Name the blood parasite species.
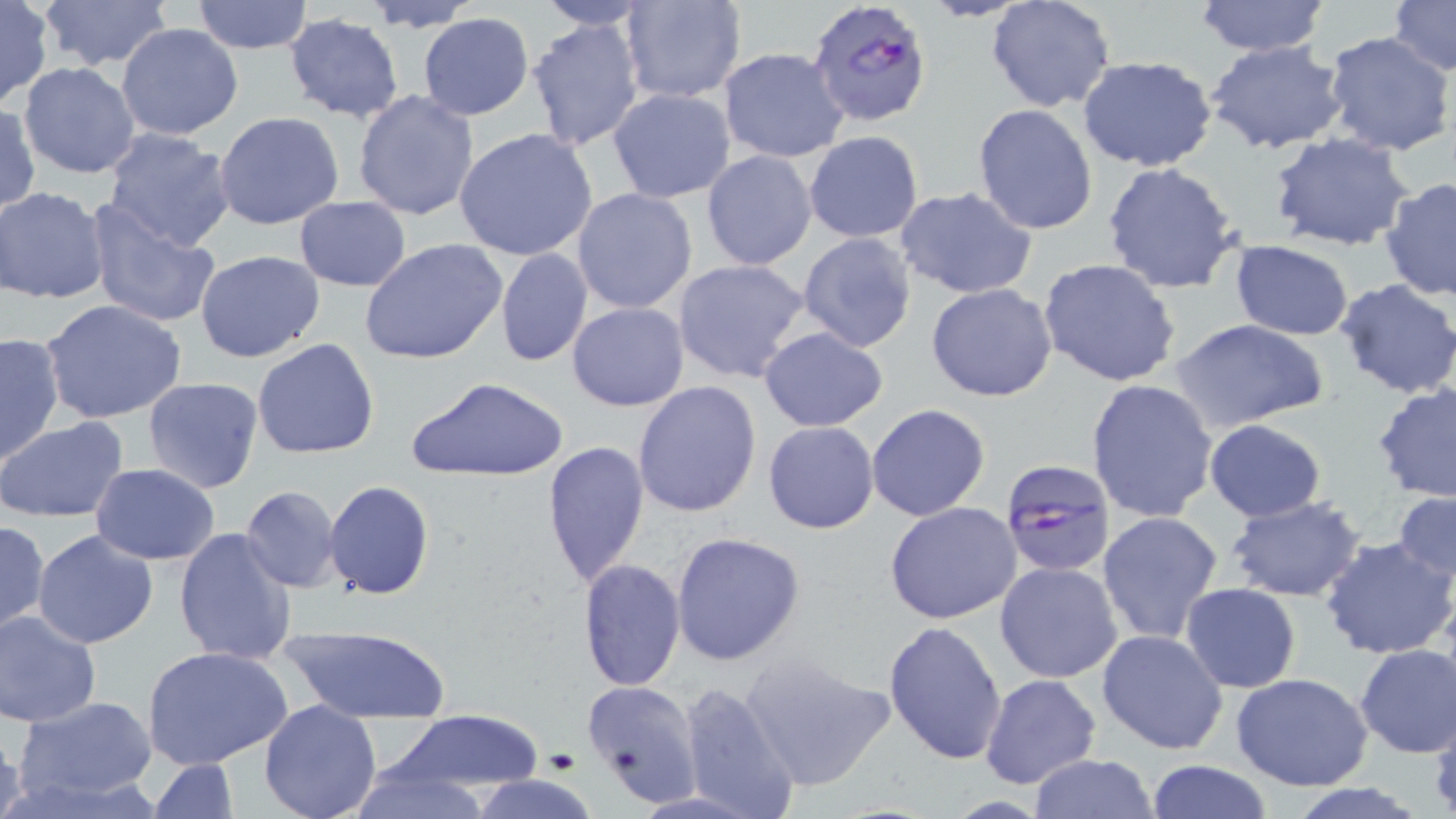

Plasmodium falciparum.

magnification = 1000x
field of view = one of a larger specimen
uninfected red blood cell locations = approximate bounding boxes as (x1,y1)-(x2,y2) corner pairs in pixels: (35,0)-(174,70), (534,0)-(655,30), (619,0)-(747,103), (985,0)-(1116,114), (1192,0)-(1331,56), (1386,0)-(1455,74), (192,1)-(312,52), (362,1)-(482,32), (0,3)-(50,106), (416,12)-(534,120), (283,15)-(406,123), (526,16)-(644,154), (117,21)-(244,142), (1323,32)-(1456,158), (1205,39)-(1348,155), (719,48)-(849,162), (1076,54)-(1219,172), (19,62)-(141,180), (607,88)-(737,204), (353,90)-(479,220), (972,103)-(1099,235), (1,105)-(40,216), (214,112)-(345,230), (454,127)-(597,262), (102,128)-(236,252), (805,131)-(923,242), (1266,131)-(1415,253), (701,150)-(818,271), (1101,161)-(1244,296), (1379,177)-(1456,301), (1,185)-(111,305), (896,185)-(1038,301), (571,187)-(698,315), (294,197)-(411,290), (84,202)-(221,328), (798,231)-(919,353), (360,237)-(507,365), (1229,240)-(1355,340), (495,249)-(593,366), (195,250)-(327,363), (672,258)-(811,384), (1037,258)-(1183,388), (1334,278)-(1456,399), (926,283)-(1058,403), (41,300)-(189,424), (567,302)-(689,411), (1170,318)-(1328,432), (758,327)-(889,432), (0,331)-(65,466), (252,338)-(380,459), (407,376)-(568,480), (142,377)-(266,495), (1086,379)-(1220,524), (632,381)-(762,520), (1370,382)-(1456,501), (867,402)-(991,522), (0,415)-(130,525), (1203,418)-(1327,522), (762,421)-(881,534), (543,439)-(650,590), (91,464)-(220,563), (325,480)-(436,600), (240,485)-(342,592), (1392,489)-(1455,589), (1222,495)-(1368,602), (884,501)-(1024,624), (1097,511)-(1225,647), (0,519)-(49,636), (174,527)-(297,666), (32,529)-(159,649), (670,531)-(806,666), (1320,535)-(1456,660), (579,559)-(685,691), (994,561)-(1124,684), (1181,583)-(1301,694), (0,610)-(101,726), (883,620)-(1008,765), (280,621)-(452,723), (1097,629)-(1230,755), (1355,644)-(1456,758), (142,645)-(296,772), (738,651)-(894,792), (980,673)-(1102,790), (1230,673)-(1373,790), (678,678)-(803,819), (583,679)-(703,804), (14,696)-(158,804), (259,700)-(383,819), (390,709)-(546,795), (1,719)-(27,819), (1027,754)-(1160,819), (149,759)-(240,817), (1143,760)-(1274,818), (348,762)-(490,819), (468,774)-(598,819)
Plasmodium falciparum-infected red blood cell locations = approximate bounding boxes as (x1,y1)-(x2,y2) corner pairs in pixels: (805,0)-(933,129), (997,456)-(1118,579)
preparation = thin blood film
image size = 1456×819 pixels
modality = optical microscopy
stain = May-Grünwald-Giemsa